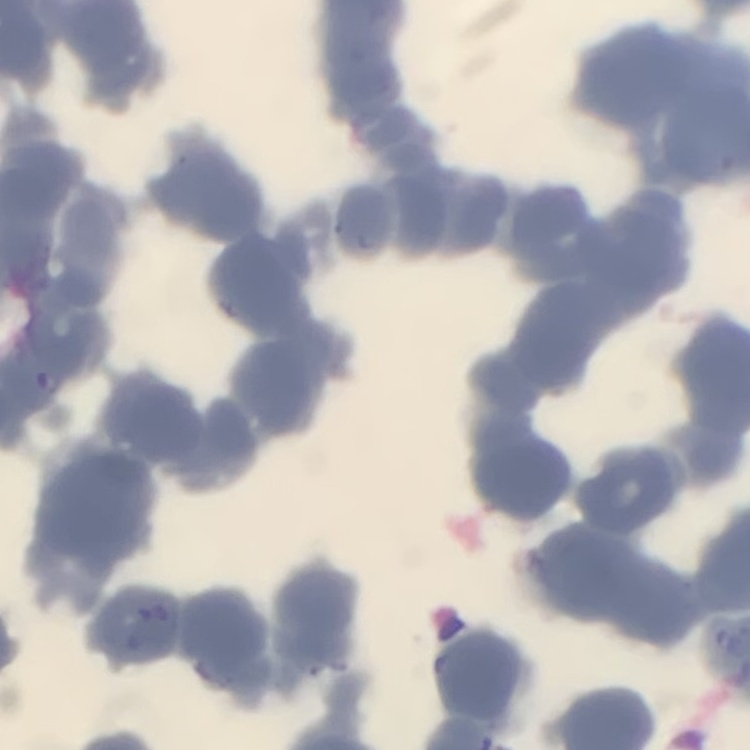

Summary:
  - Erythrocyte morphology: rouleaux formation
  - Preparation: thin blood film
  - Image type: one tile cut from a larger photomicrograph
  - Stain: Field's or Giemsa